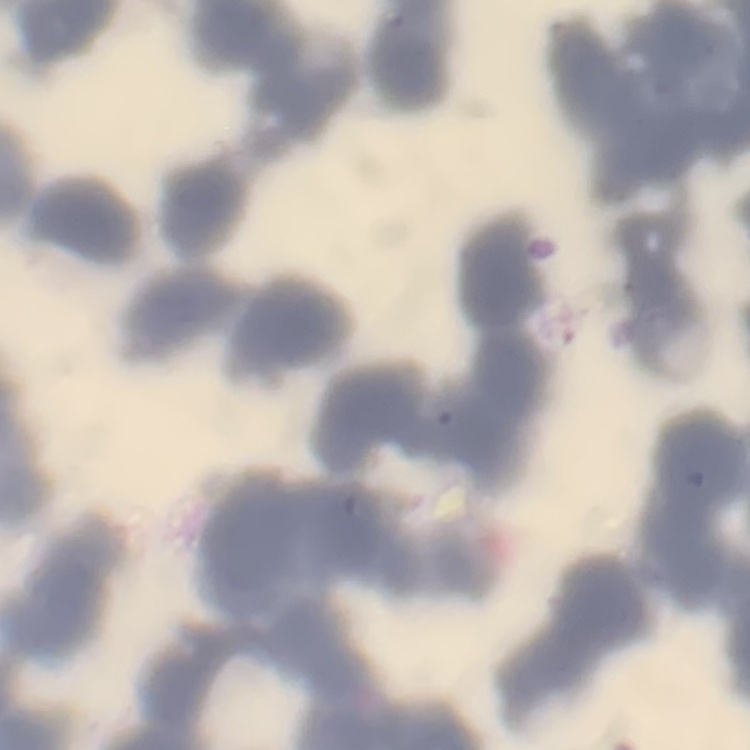

red_blood_cell_morphology: rouleaux formation
preparation: thin peripheral smear
image_type: one tile cut from a larger photomicrograph
stain: Field's or Giemsa